Describe the morphology of the erythrocytes.
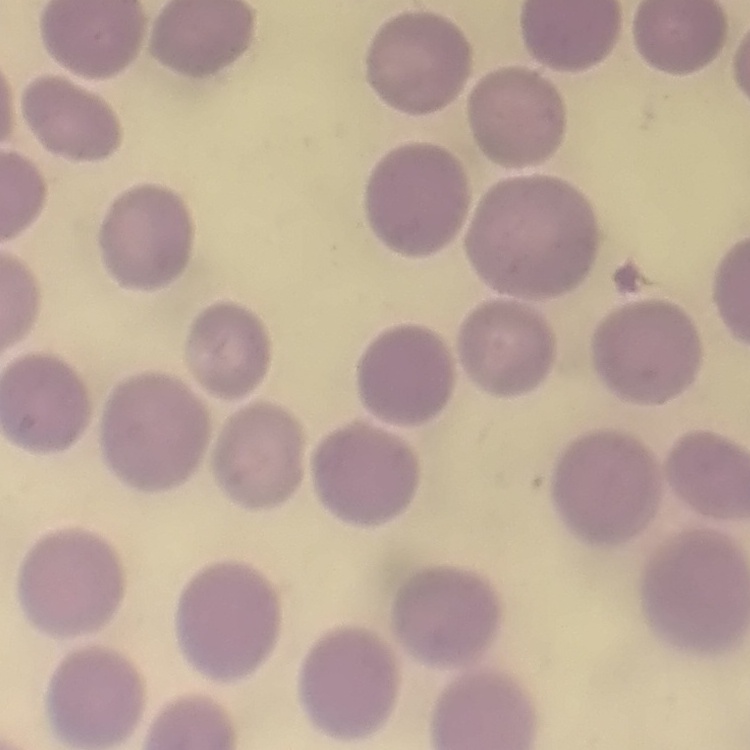

No rouleaux formation.

Summary:
  - Stain: Field's or Giemsa
  - Image type: square crop of a larger photomicrograph
  - Preparation: thin blood film